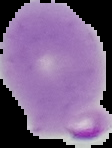

image type = segmented cell region on a black background
preparation = thin blood film
image size = 112×148 pixels
malaria status = parasitized